Locate every blood parasite and identify its species.
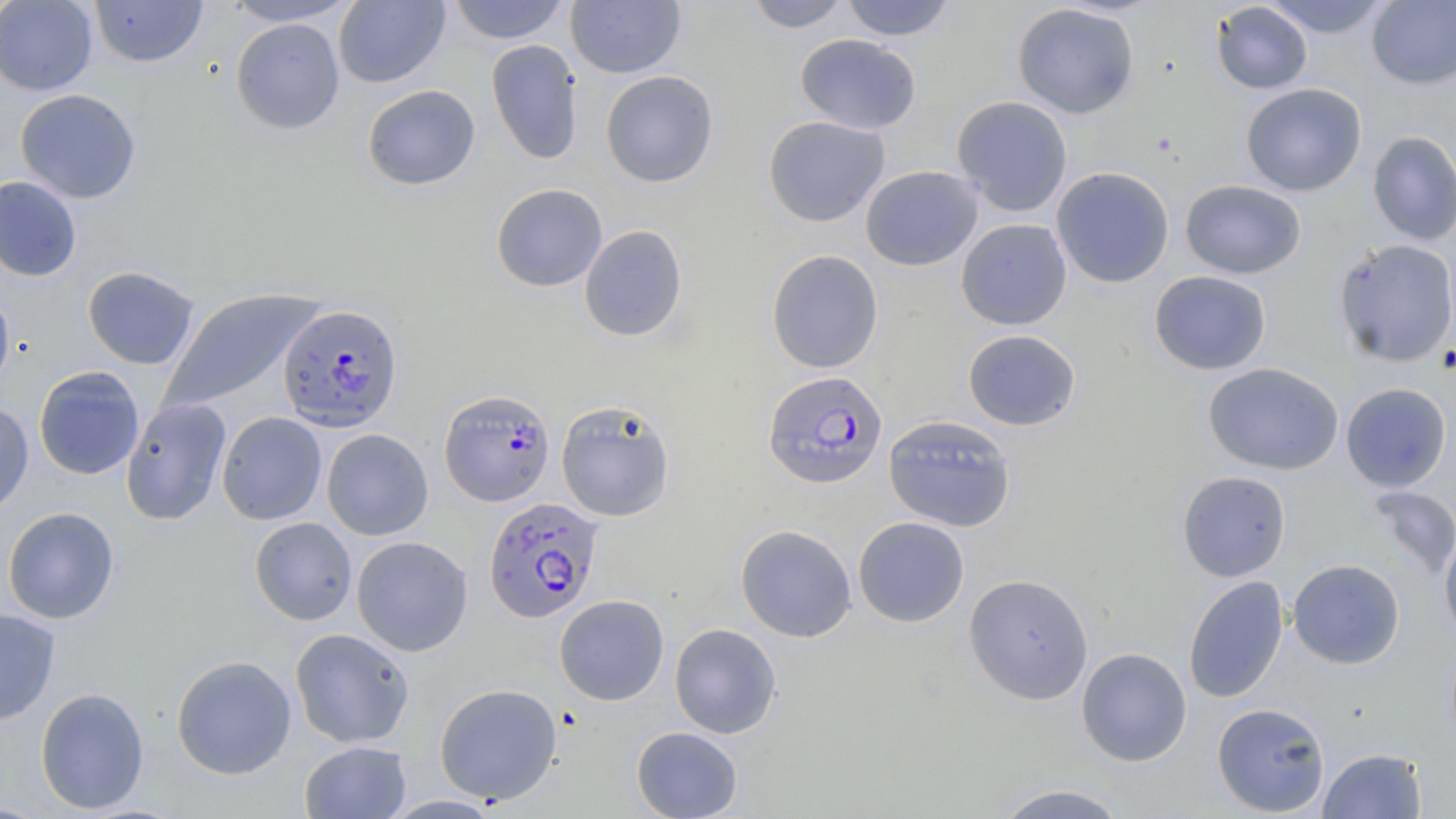
Approximate bounding boxes as named x1/y1/x2/y2 corners in pixels.
Plasmodium falciparum-infected red blood cells: (x1=277, y1=304, x2=403, y2=432), (x1=762, y1=370, x2=888, y2=489), (x1=439, y1=389, x2=556, y2=506), (x1=484, y1=497, x2=603, y2=622).
No Plasmodium ovale, Plasmodium malariae, Plasmodium vivax, Babesia divergens, or Trypanosoma brucei observed.

{
  "slide_level_diagnosis": "Plasmodium falciparum",
  "field_of_view": "one of a larger specimen",
  "uninfected_red_blood_cell_locations": "approximate bounding boxes as named x1/y1/x2/y2 corners in pixels: (x1=89, y1=0, x2=208, y2=68), (x1=222, y1=0, x2=362, y2=26), (x1=334, y1=0, x2=451, y2=88), (x1=447, y1=0, x2=570, y2=44), (x1=566, y1=0, x2=686, y2=78), (x1=745, y1=0, x2=852, y2=32), (x1=839, y1=0, x2=958, y2=41), (x1=1261, y1=0, x2=1393, y2=38), (x1=1367, y1=0, x2=1456, y2=90), (x1=0, y1=1, x2=98, y2=95), (x1=1211, y1=2, x2=1313, y2=95), (x1=1012, y1=3, x2=1140, y2=118), (x1=231, y1=17, x2=345, y2=134), (x1=795, y1=34, x2=921, y2=135), (x1=486, y1=39, x2=584, y2=164), (x1=600, y1=70, x2=719, y2=187), (x1=1241, y1=83, x2=1367, y2=196), (x1=362, y1=84, x2=481, y2=191), (x1=15, y1=88, x2=141, y2=204), (x1=951, y1=96, x2=1073, y2=216), (x1=763, y1=115, x2=890, y2=227), (x1=1368, y1=130, x2=1456, y2=245), (x1=860, y1=165, x2=983, y2=271), (x1=1051, y1=167, x2=1174, y2=288), (x1=0, y1=176, x2=82, y2=281), (x1=1180, y1=180, x2=1306, y2=279), (x1=491, y1=183, x2=608, y2=291), (x1=956, y1=218, x2=1072, y2=330), (x1=579, y1=224, x2=688, y2=342), (x1=1334, y1=239, x2=1456, y2=366), (x1=766, y1=249, x2=884, y2=373), (x1=82, y1=266, x2=200, y2=369), (x1=1149, y1=270, x2=1272, y2=375), (x1=0, y1=283, x2=16, y2=402), (x1=159, y1=288, x2=323, y2=414), (x1=963, y1=329, x2=1081, y2=431), (x1=1203, y1=362, x2=1344, y2=476), (x1=33, y1=365, x2=145, y2=480), (x1=1340, y1=382, x2=1452, y2=492), (x1=120, y1=397, x2=232, y2=526), (x1=555, y1=399, x2=676, y2=522), (x1=0, y1=401, x2=34, y2=516), (x1=217, y1=412, x2=327, y2=525), (x1=883, y1=414, x2=1016, y2=532), (x1=321, y1=429, x2=433, y2=540), (x1=1177, y1=470, x2=1291, y2=582), (x1=1368, y1=486, x2=1456, y2=580), (x1=2, y1=506, x2=120, y2=624), (x1=853, y1=516, x2=970, y2=627), (x1=249, y1=517, x2=358, y2=625), (x1=735, y1=524, x2=857, y2=642), (x1=1440, y1=528, x2=1456, y2=643), (x1=352, y1=536, x2=473, y2=656), (x1=1287, y1=559, x2=1405, y2=669), (x1=964, y1=573, x2=1093, y2=703), (x1=1183, y1=575, x2=1288, y2=703), (x1=554, y1=594, x2=669, y2=705), (x1=0, y1=607, x2=61, y2=725), (x1=669, y1=623, x2=782, y2=739), (x1=290, y1=628, x2=415, y2=747), (x1=1076, y1=647, x2=1192, y2=766), (x1=171, y1=655, x2=297, y2=779), (x1=434, y1=683, x2=562, y2=805), (x1=35, y1=687, x2=150, y2=813), (x1=1212, y1=702, x2=1330, y2=816), (x1=631, y1=726, x2=743, y2=818), (x1=299, y1=741, x2=411, y2=819), (x1=1317, y1=748, x2=1427, y2=819), (x1=992, y1=783, x2=1129, y2=819)",
  "stain": "May-Grünwald-Giemsa",
  "preparation": "thin blood smear",
  "image_size": "1456×819 pixels",
  "modality": "light microscopy",
  "magnification": "1000x"
}